Name the parasite shown.
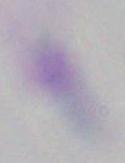
Toxoplasma gondii.

Summary:
  - Magnification: 1000x
  - Modality: micrograph